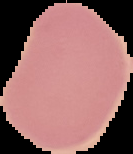
Summary:
  - Malaria status: uninfected
  - Image type: segmented cell region with the area outside set to black
  - Preparation: thin blood film
  - Image size: 133×154 pixels